Assess the morphology of the red blood cells.
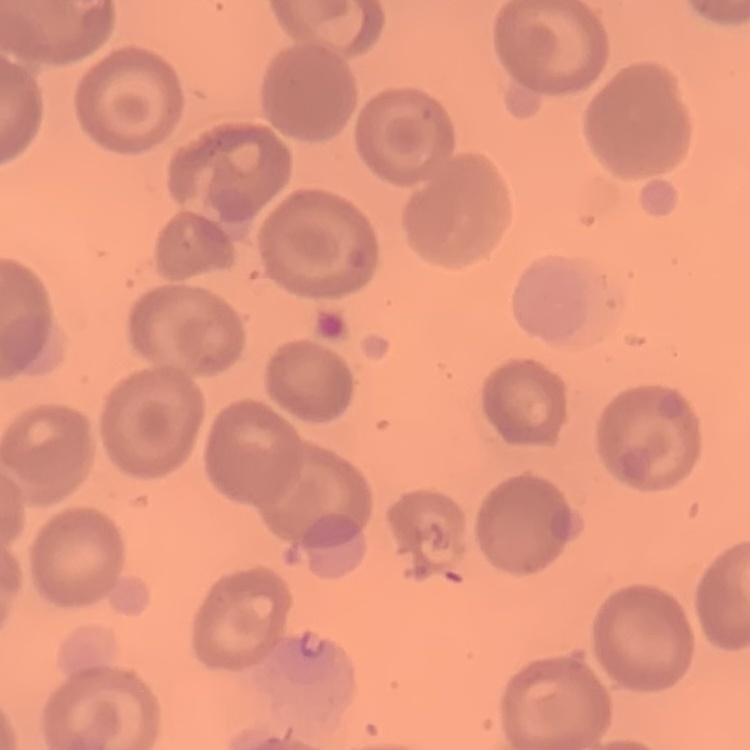

They show no rouleaux formation.

stain = Field's or Giemsa
image type = square crop of a larger photomicrograph
preparation = thin blood film